Assess this cell for malaria.
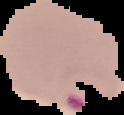

Parasitized.

Summary:
  - Image type: cell region segmented out of the field of view; surrounding area masked to black
  - Image size: 124×115 pixels
  - Preparation: thin blood smear